Report the malaria status of this cell.
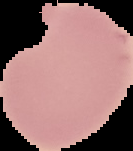

Uninfected.

From a thin blood film. The area outside the segmented cell region is set to black. Image is 133×151 pixels.